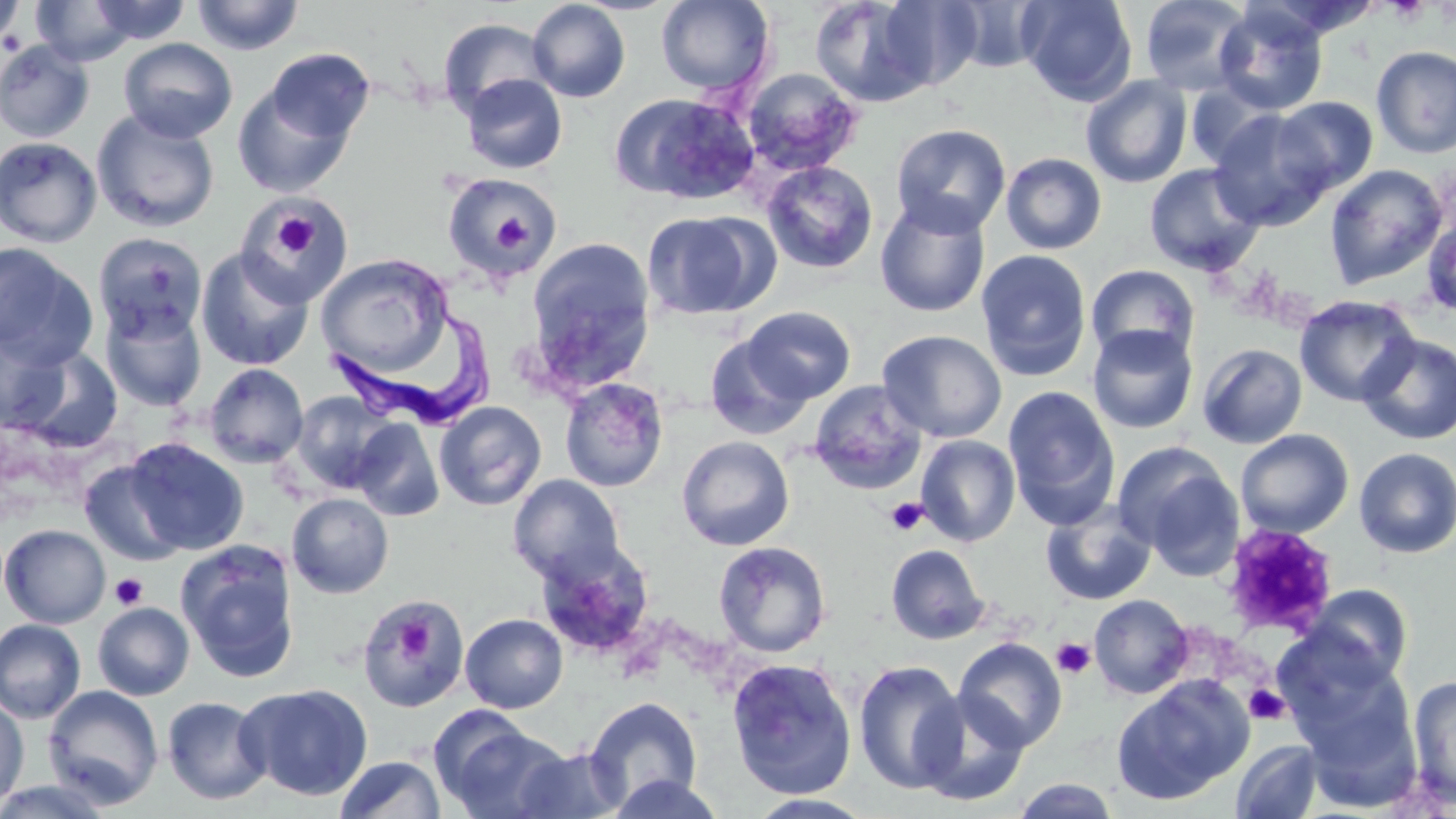 Approximate bounding boxes as (x1,y1)-(x2,y2) corner pairs in pixels. Platelet locations: (1384,0)-(1430,22), (484,206)-(532,253), (268,209)-(322,262), (886,497)-(928,535), (1221,523)-(1338,637), (110,572)-(148,610), (360,598)-(466,710), (395,617)-(433,660), (1051,637)-(1096,678), (1244,684)-(1288,724). Trypanosoma brucei locations: (326,317)-(498,431). Uninfected red blood cell locations: (190,0)-(306,55), (655,0)-(775,95), (807,0)-(948,107), (1017,0)-(1137,106), (1138,0)-(1256,95), (0,1)-(27,49), (29,1)-(142,67), (86,1)-(192,45), (527,1)-(631,103), (945,1)-(1050,73), (1212,3)-(1329,116), (437,18)-(554,120), (118,37)-(238,143), (0,39)-(95,144), (1372,45)-(1456,158), (264,47)-(375,146), (741,67)-(864,176), (461,73)-(567,174), (1081,74)-(1192,188), (231,80)-(358,199), (1185,81)-(1284,171), (611,93)-(758,203), (1273,97)-(1378,195), (1208,108)-(1335,230), (92,109)-(220,233), (890,123)-(1011,237), (0,137)-(102,249), (1001,152)-(1107,255), (760,160)-(879,275), (1144,163)-(1265,276), (1324,163)-(1448,290), (443,173)-(561,279), (238,196)-(353,306), (874,196)-(991,318), (1421,209)-(1456,321), (641,211)-(772,320), (93,232)-(208,342), (526,237)-(655,386), (0,243)-(97,369), (195,248)-(315,371), (976,249)-(1092,381), (315,253)-(454,375), (1086,263)-(1200,365), (1294,295)-(1420,407), (100,302)-(207,412), (741,305)-(855,404), (1087,324)-(1198,435), (0,330)-(69,432), (877,330)-(1008,443), (705,333)-(811,439), (1358,334)-(1456,445), (1197,343)-(1308,449), (14,346)-(123,453), (203,363)-(309,468), (559,377)-(669,492), (808,380)-(928,495), (1003,384)-(1120,529), (291,391)-(396,494), (434,401)-(547,510), (352,418)-(445,522), (1235,429)-(1354,538), (676,435)-(795,551), (915,435)-(1021,547), (123,437)-(248,555), (1116,444)-(1244,574), (1353,447)-(1456,558), (79,459)-(187,566), (508,474)-(626,583), (286,493)-(393,598), (1041,500)-(1156,606), (1,524)-(110,628), (175,540)-(301,682), (713,540)-(831,658), (885,543)-(991,645), (1302,583)-(1413,688), (1089,594)-(1194,698), (356,598)-(468,712), (93,602)-(194,701), (460,613)-(567,713), (0,619)-(86,724), (953,637)-(1068,753), (1283,651)-(1420,788), (726,657)-(858,799), (853,659)-(967,795), (1407,675)-(1456,809), (1111,676)-(1253,806), (238,683)-(373,800), (43,685)-(164,809), (913,692)-(1031,807), (0,696)-(29,810), (161,696)-(271,805), (584,696)-(703,809), (435,718)-(570,818), (1231,739)-(1324,818), (512,745)-(629,818), (334,756)-(445,818), (604,773)-(727,818), (1009,777)-(1121,818), (0,778)-(118,819), (746,793)-(878,818). Slide-level diagnosis: Trypanosoma brucei. Image is 1456×819 pixels. May-Grünwald-Giemsa stain. Captured at 1000x magnification. Single field of view. Thin blood smear. Optical microscopy.